Comment on the morphology of the erythrocytes.
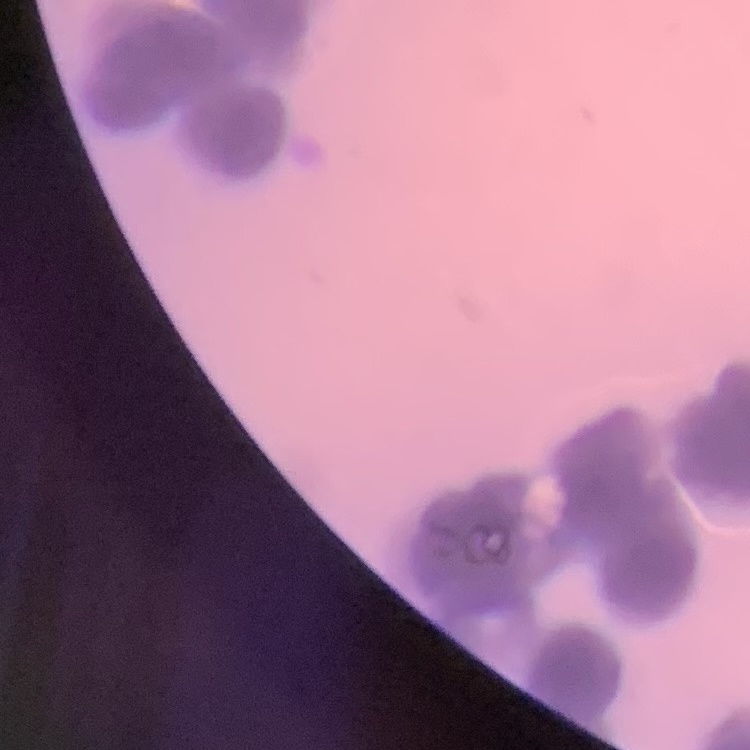
Rouleaux formation.

Thin blood film. One tile cut from a larger photomicrograph. Field's or Giemsa stain.